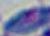
1000x magnification. Photomicrograph. Toxoplasma gondii is seen.